Assess this cell for malaria.
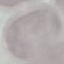

Uninfected.

Automatically extracted cell patch, resized to 64 × 64 pixels. Thin smear of blood. Acquired by smartphone through the microscope eyepiece. Giemsa stain.